Give the position of every leukocyte visible.
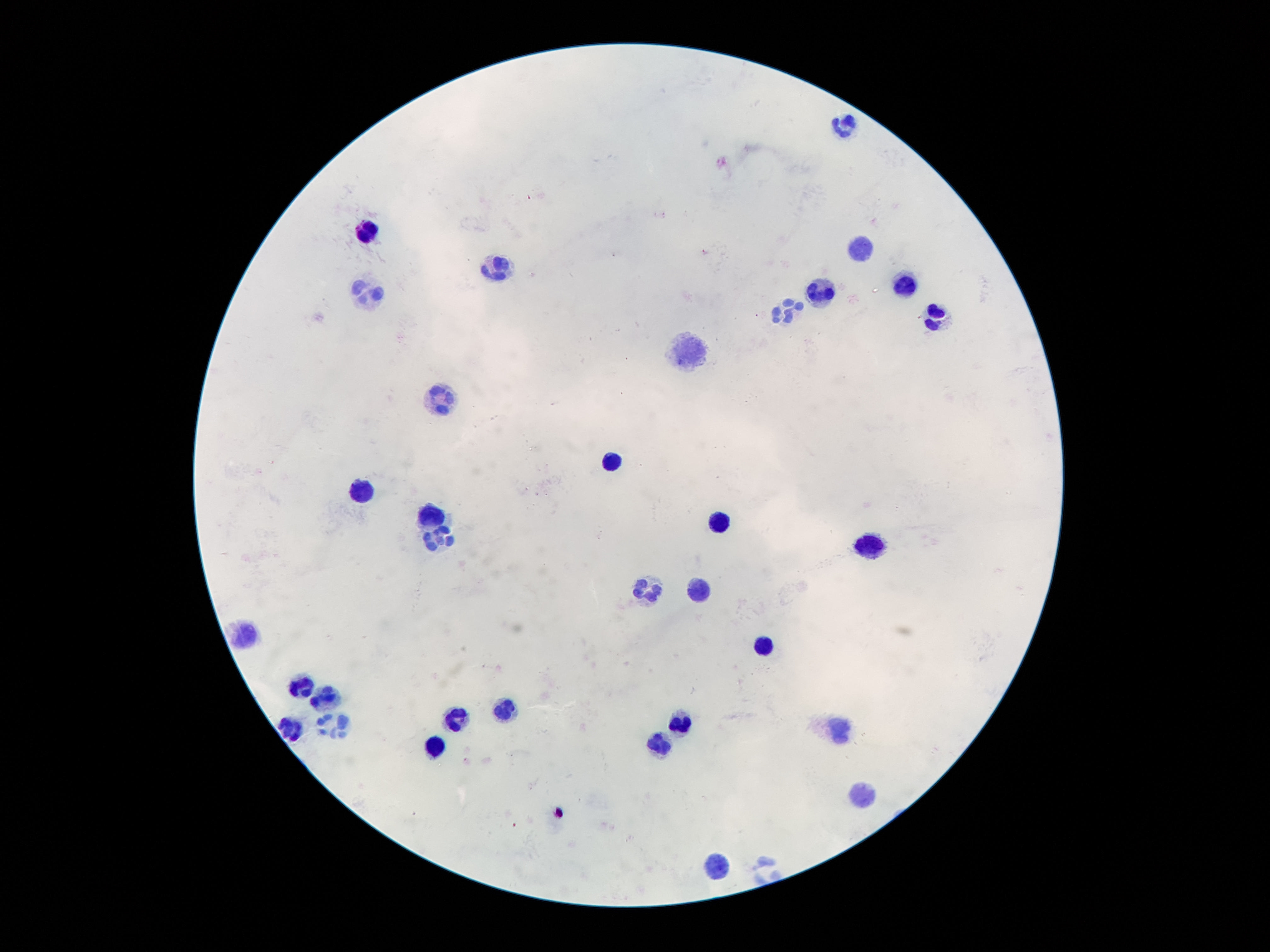

Approximate centers as (x, y) in pixels.
Leukocytes: (842, 125), (361, 230), (859, 247), (498, 273), (823, 288), (901, 288), (367, 290), (787, 312), (934, 319), (687, 357), (441, 401), (611, 462), (363, 491), (433, 515), (720, 520), (441, 537), (869, 546), (647, 588), (699, 590), (241, 634), (762, 644), (305, 686), (325, 698), (504, 709), (454, 716), (680, 718), (332, 725), (290, 728), (840, 730), (659, 743), (435, 746), (859, 798), (712, 866).

Patient malaria status: uninfected. Thick blood film. 100x magnification. Smartphone photograph taken through the microscope eyepiece. Image is 1270×952 pixels. Giemsa stain. One field from this slide.